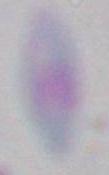

Captured at 1000x magnification. Toxoplasma gondii is shown. Micrograph.